Report the malaria status of this cell.
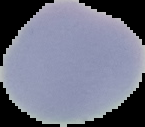

Uninfected.

From a thin blood film. Cell region segmented out of the field of view; the surrounding area is masked to black. Image is 145×127 pixels.